Comment on the morphology of the red blood cells.
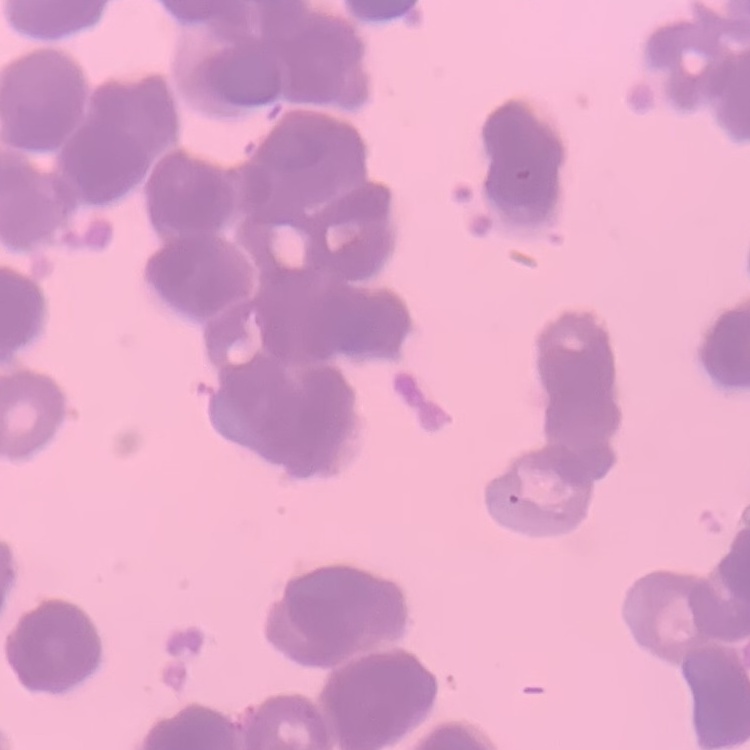
Rouleaux formation.

image type = one tile cut from a larger photomicrograph
preparation = thin blood film
stain = Field's or Giemsa